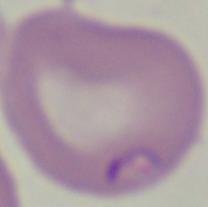

Summary:
  - Identification: Babesia
  - Modality: photomicrograph
  - Magnification: 1000x